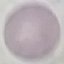
{
  "malaria_status": "uninfected",
  "stain": "Giemsa",
  "capture": "smartphone through the microscope eyepiece",
  "image_type": "cell patch, automatically extracted from a larger field of view and resized to 64 × 64 pixels",
  "preparation": "thin blood film"
}